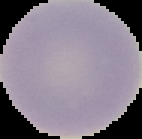
Image is 142×139 pixels. Segmented cell region on a black background. Result: no Plasmodium parasites detected. From a thin blood film.